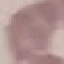
Malaria status: uninfected. Thin blood film. Photographed with a smartphone camera at the microscope eyepiece. Giemsa-stained preparation. Cell patch, automatically extracted from a larger field of view and resized to 64 × 64 pixels.